Assess this cell for malaria.
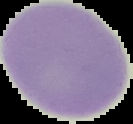
Uninfected.

Summary:
  - Preparation: thin blood film
  - Image size: 133×124 pixels
  - Image type: segmented cell region with the area outside set to black